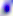
identification = Toxoplasma gondii
modality = photomicrograph
magnification = 400x